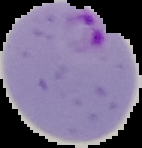

image type = cell region segmented out of the field of view; surrounding area masked to black
image size = 142×148 pixels
preparation = thin blood smear
malaria status = parasitized